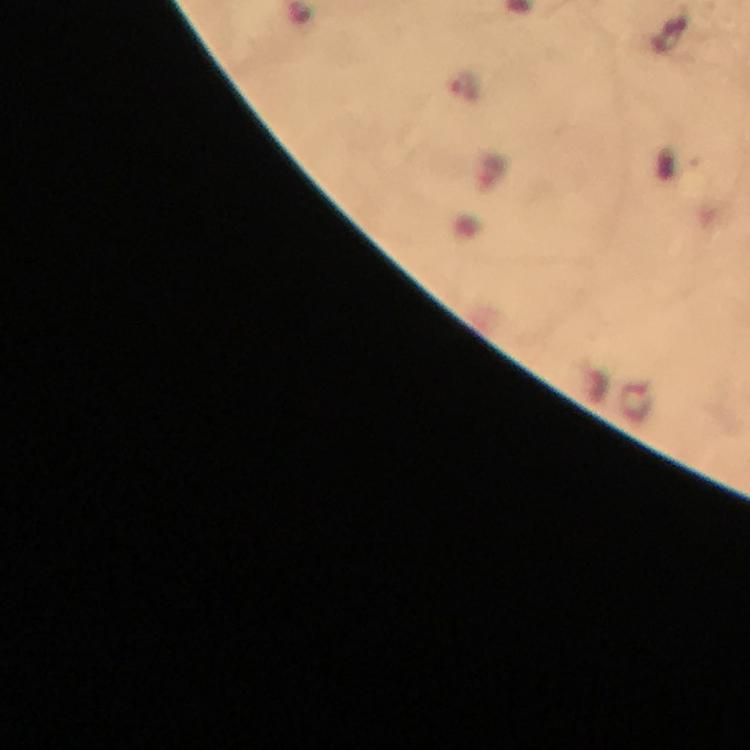
image size = 750×750 pixels
immersion oil = used
magnification = 100x
context = from a diagnostic examination for malaria
stain = Giemsa
capture = smartphone mounted on the microscope
preparation = thick blood film
cropped from = a single field of view
malaria parasite locations = approximate centers as (x, y) in pixels: (465, 87)